Locate platelets.
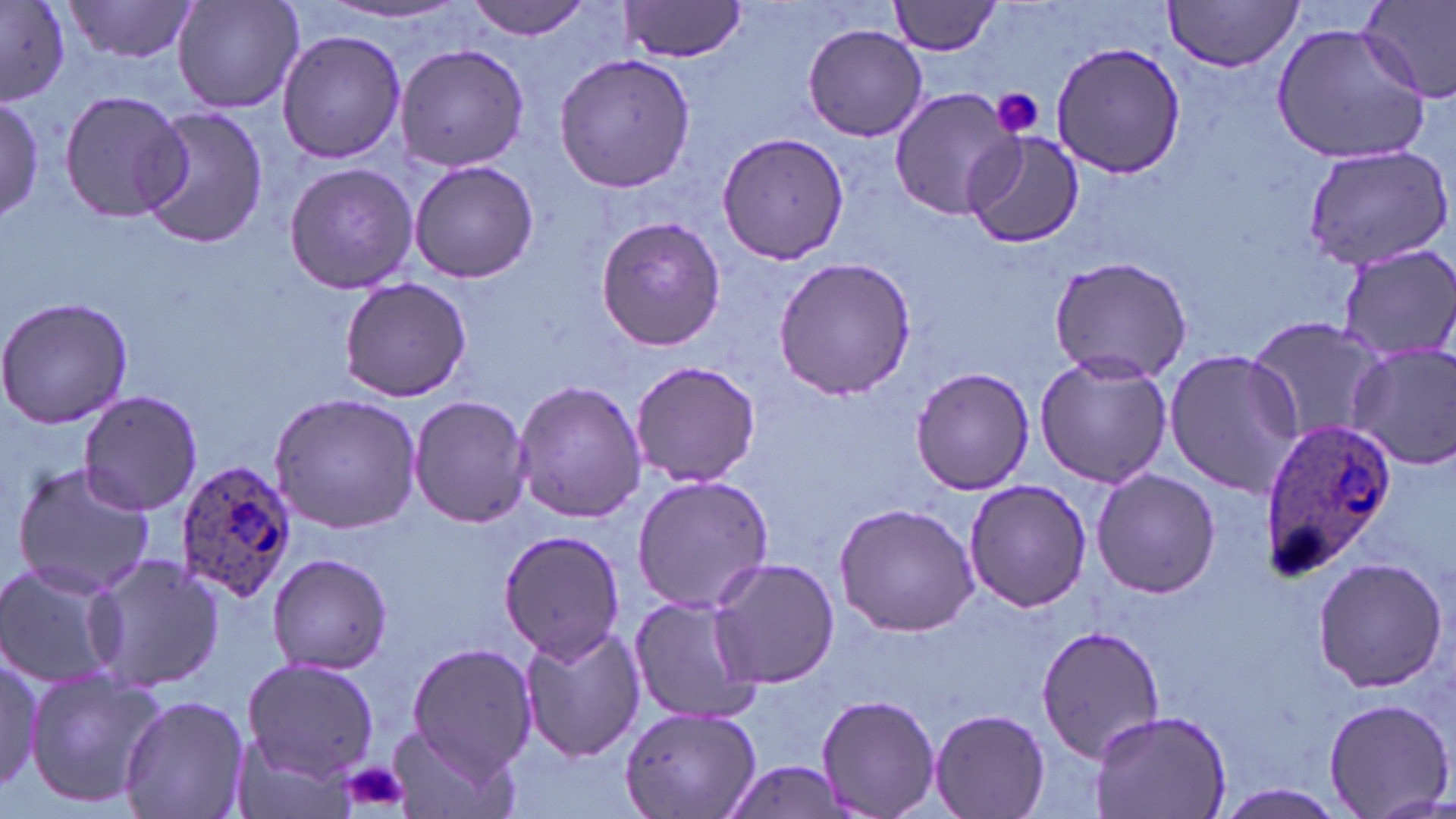

Approximate bounding boxes as named x1/y1/x2/y2 corners in pixels.
Platelets: (x1=991, y1=89, x2=1044, y2=139), (x1=338, y1=758, x2=411, y2=814).

Summary:
  - Uninfected red blood cell locations: (x1=61, y1=0, x2=200, y2=63), (x1=174, y1=0, x2=304, y2=115), (x1=464, y1=0, x2=596, y2=39), (x1=617, y1=0, x2=748, y2=63), (x1=888, y1=0, x2=1006, y2=56), (x1=1161, y1=0, x2=1304, y2=71), (x1=1360, y1=0, x2=1456, y2=103), (x1=0, y1=2, x2=75, y2=103), (x1=319, y1=4, x2=470, y2=25), (x1=1272, y1=20, x2=1431, y2=166), (x1=803, y1=23, x2=928, y2=142), (x1=275, y1=29, x2=406, y2=165), (x1=1051, y1=34, x2=1186, y2=176), (x1=394, y1=43, x2=529, y2=172), (x1=551, y1=52, x2=697, y2=194), (x1=887, y1=86, x2=1025, y2=220), (x1=60, y1=89, x2=190, y2=223), (x1=0, y1=94, x2=47, y2=226), (x1=137, y1=104, x2=268, y2=250), (x1=965, y1=130, x2=1086, y2=248), (x1=716, y1=131, x2=850, y2=265), (x1=1299, y1=141, x2=1454, y2=274), (x1=408, y1=159, x2=539, y2=283), (x1=282, y1=161, x2=417, y2=294), (x1=595, y1=214, x2=728, y2=351), (x1=1334, y1=243, x2=1456, y2=365), (x1=1047, y1=254, x2=1193, y2=385), (x1=771, y1=255, x2=919, y2=403), (x1=338, y1=276, x2=474, y2=404), (x1=0, y1=295, x2=134, y2=430), (x1=1246, y1=312, x2=1394, y2=447), (x1=1345, y1=342, x2=1456, y2=468), (x1=1164, y1=347, x2=1302, y2=497), (x1=1033, y1=352, x2=1172, y2=489), (x1=629, y1=358, x2=763, y2=488), (x1=909, y1=366, x2=1034, y2=496), (x1=512, y1=378, x2=646, y2=523), (x1=76, y1=390, x2=202, y2=517), (x1=267, y1=392, x2=422, y2=533), (x1=408, y1=393, x2=531, y2=527), (x1=9, y1=460, x2=158, y2=598), (x1=1092, y1=466, x2=1218, y2=599), (x1=631, y1=474, x2=775, y2=613), (x1=962, y1=478, x2=1094, y2=614), (x1=833, y1=501, x2=980, y2=637), (x1=497, y1=528, x2=629, y2=664), (x1=267, y1=552, x2=394, y2=676), (x1=86, y1=554, x2=227, y2=692), (x1=1312, y1=557, x2=1447, y2=691), (x1=705, y1=558, x2=842, y2=687), (x1=0, y1=560, x2=127, y2=692), (x1=628, y1=596, x2=762, y2=725), (x1=516, y1=621, x2=646, y2=765), (x1=1035, y1=623, x2=1167, y2=762), (x1=405, y1=642, x2=537, y2=777), (x1=0, y1=647, x2=50, y2=799), (x1=242, y1=656, x2=378, y2=782), (x1=24, y1=666, x2=166, y2=811), (x1=118, y1=694, x2=250, y2=819), (x1=815, y1=695, x2=941, y2=819), (x1=1322, y1=697, x2=1452, y2=818), (x1=618, y1=706, x2=762, y2=819), (x1=929, y1=707, x2=1050, y2=818), (x1=1084, y1=710, x2=1233, y2=819), (x1=384, y1=723, x2=518, y2=819), (x1=719, y1=756, x2=855, y2=819), (x1=1217, y1=785, x2=1351, y2=818)
  - Plasmodium ovale-infected red blood cell locations: (x1=1259, y1=415, x2=1393, y2=580), (x1=174, y1=457, x2=300, y2=602)
  - Slide-level diagnosis: Plasmodium ovale
  - Modality: optical microscopy
  - Preparation: thin blood smear
  - Field of view: one of a larger specimen
  - Magnification: 1000x
  - Stain: May-Grünwald-Giemsa
  - Image size: 1456×819 pixels